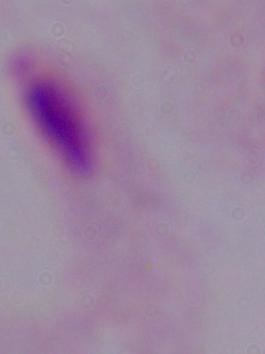

1000x magnification. Micrograph. A trichomonad is seen.